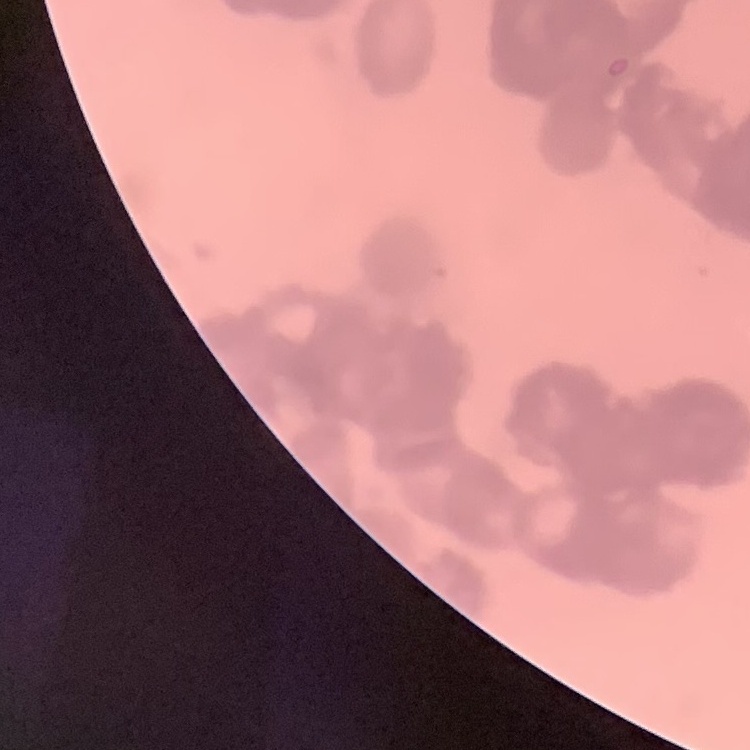

The red blood cells exhibit rouleaux formation. One tile cut from a larger photomicrograph. Thin blood film. Stained with either Field's or Giemsa.